Assess this cell for malaria.
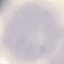

It is uninfected.

Summary:
  - Stain: Giemsa
  - Image type: cell patch, automatically extracted from a larger field of view and resized to 64 × 64 pixels
  - Preparation: thin smear
  - Capture: smartphone camera at the microscope eyepiece